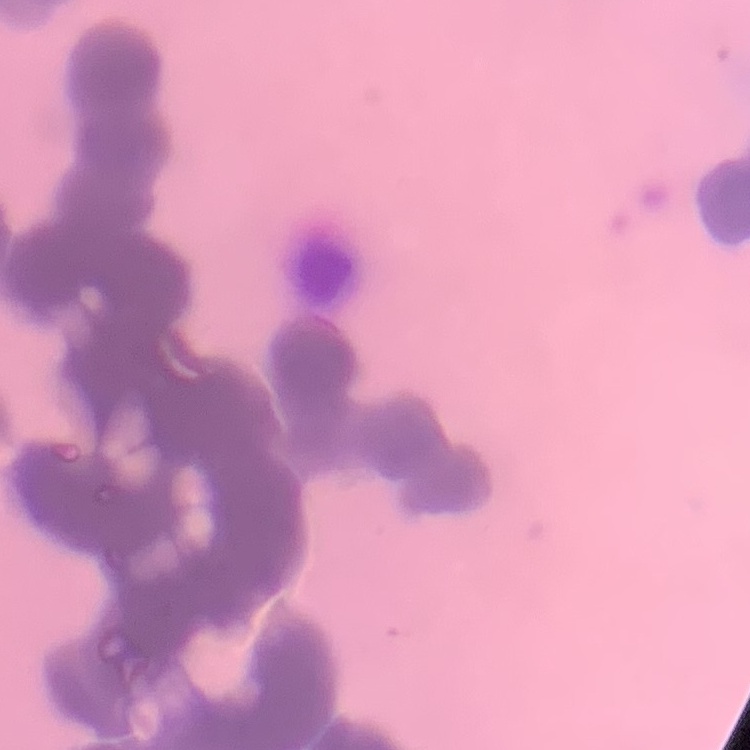

The erythrocytes exhibit rouleaux formation. Square crop of a larger photomicrograph. Thin blood film. Field's or Giemsa stain.